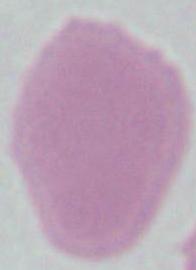 An erythrocyte is seen. Photomicrograph. Captured at 1000x magnification.